Give the extent of all uninfected red blood cells.
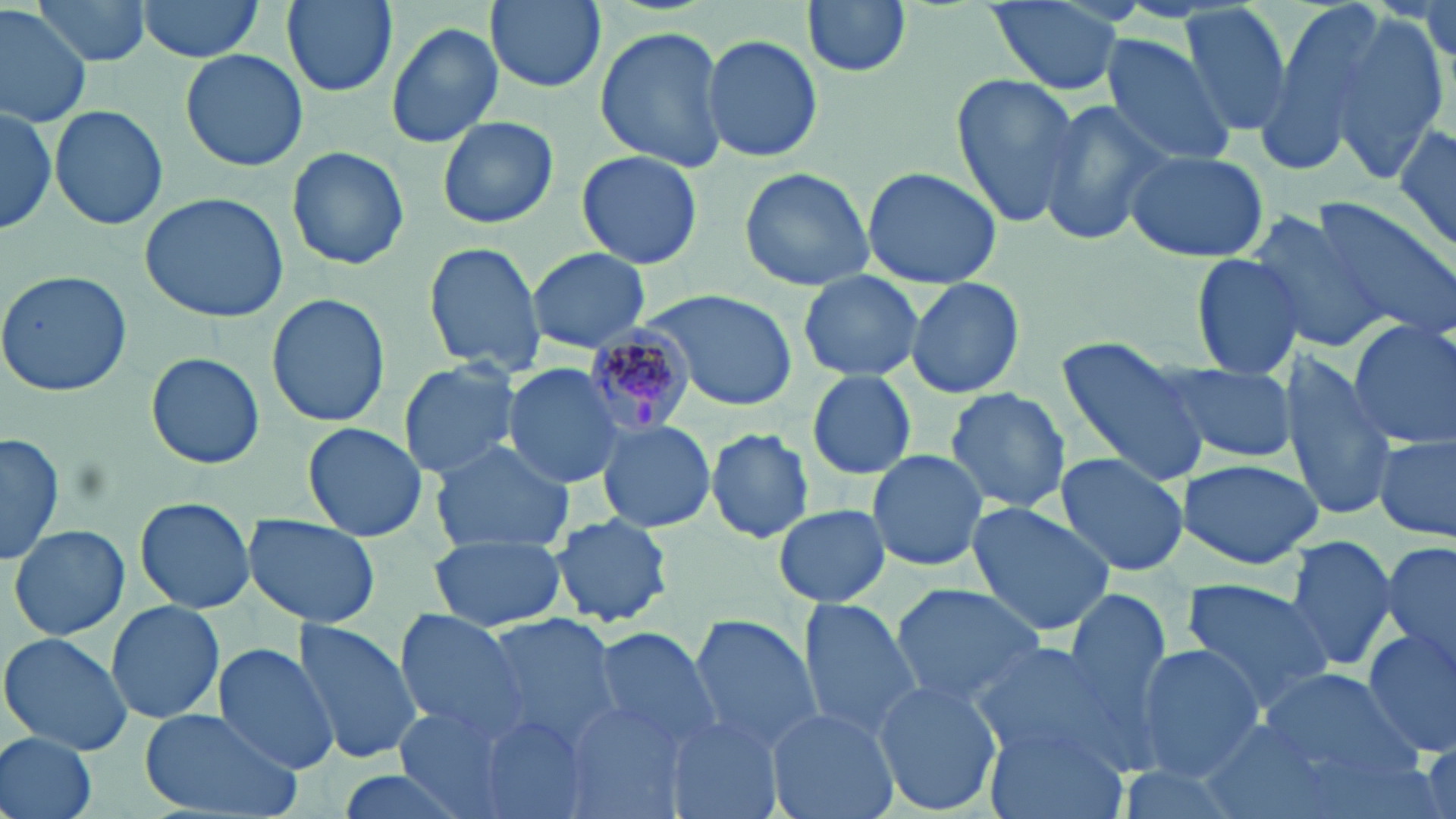

Approximate bounding boxes as (x1, y1, x2, y2) in pixels.
Uninfected red blood cells: (31, 0, 151, 67), (133, 0, 267, 62), (275, 0, 401, 99), (481, 0, 609, 95), (802, 0, 913, 77), (982, 0, 1128, 98), (1179, 3, 1295, 137), (1250, 3, 1392, 171), (0, 5, 92, 129), (1419, 5, 1453, 63), (1329, 13, 1450, 183), (384, 21, 504, 149), (594, 26, 731, 173), (701, 31, 823, 164), (1098, 35, 1238, 169), (179, 47, 308, 172), (948, 74, 1082, 227), (1037, 98, 1173, 248), (1, 99, 60, 237), (49, 102, 169, 231), (438, 115, 558, 229), (1393, 124, 1456, 253), (287, 145, 410, 271), (575, 149, 703, 271), (1125, 149, 1269, 264), (737, 165, 876, 291), (861, 166, 1001, 287), (138, 192, 290, 323), (1311, 199, 1456, 342), (1243, 208, 1392, 355), (423, 243, 546, 375), (526, 247, 651, 352), (1191, 249, 1308, 380), (0, 270, 132, 396), (797, 270, 924, 383), (905, 276, 1025, 400), (645, 287, 797, 411), (266, 294, 390, 429), (1348, 319, 1456, 450), (1055, 338, 1213, 487), (146, 352, 264, 468), (1278, 356, 1394, 520), (398, 360, 523, 480), (501, 362, 628, 489), (1157, 362, 1296, 462), (806, 370, 917, 480), (945, 387, 1071, 514), (596, 418, 717, 534), (302, 423, 427, 540), (704, 428, 816, 542), (2, 431, 64, 566), (1374, 434, 1454, 543), (428, 440, 575, 554), (866, 449, 990, 572), (1054, 452, 1190, 578), (1176, 457, 1323, 569), (134, 498, 256, 612), (964, 501, 1116, 638), (771, 504, 892, 606), (544, 511, 677, 630), (242, 514, 382, 629), (10, 523, 129, 641), (428, 532, 566, 632), (1281, 534, 1396, 676), (1381, 539, 1456, 684), (1180, 578, 1333, 713), (888, 583, 1049, 705), (1062, 587, 1173, 725), (797, 600, 921, 739), (105, 601, 225, 723), (392, 611, 530, 740), (476, 613, 624, 747), (687, 614, 824, 760), (291, 619, 420, 764), (586, 625, 722, 756), (1358, 628, 1456, 752), (0, 631, 132, 757), (968, 644, 1120, 760), (1131, 644, 1265, 781), (211, 646, 340, 773), (1258, 666, 1422, 784), (872, 678, 1001, 818), (555, 701, 693, 819), (393, 704, 524, 817), (766, 705, 897, 819), (138, 707, 302, 819), (471, 712, 598, 819), (1194, 715, 1333, 818), (660, 719, 780, 819), (981, 723, 1125, 819), (0, 732, 99, 819), (1107, 763, 1250, 819), (329, 767, 482, 819).

Plasmodium malariae-infected red blood cell locations: (582, 325, 697, 436). Slide-level diagnosis: Plasmodium malariae. Captured at 1000x magnification. One field of a larger specimen. Image is 1456×819 pixels. Thin blood film. May-Grünwald-Giemsa stain. Light microscopy.